Describe the morphology of the erythrocytes.
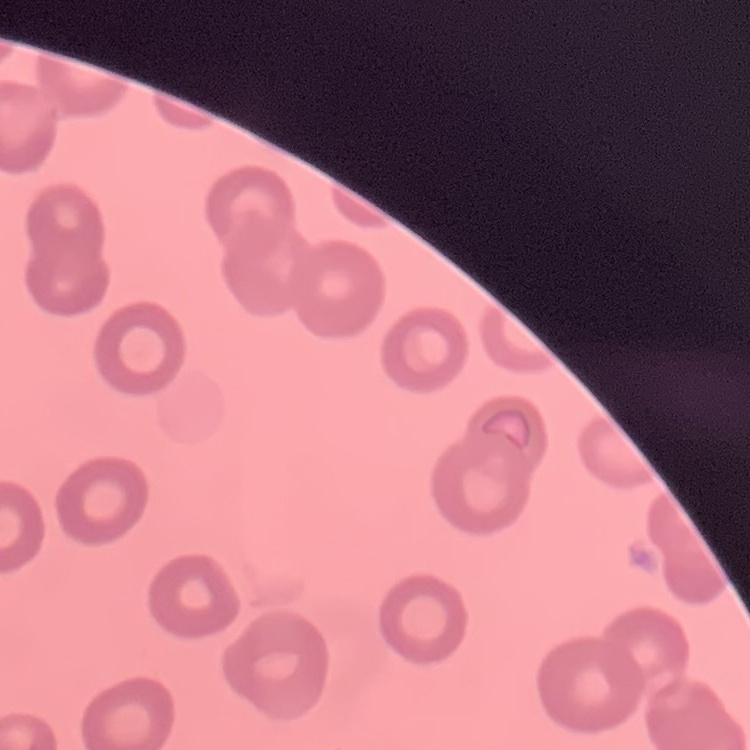
They show no rouleaux formation.

preparation = thin blood smear
image type = square crop of a larger photomicrograph
stain = Field's or Giemsa